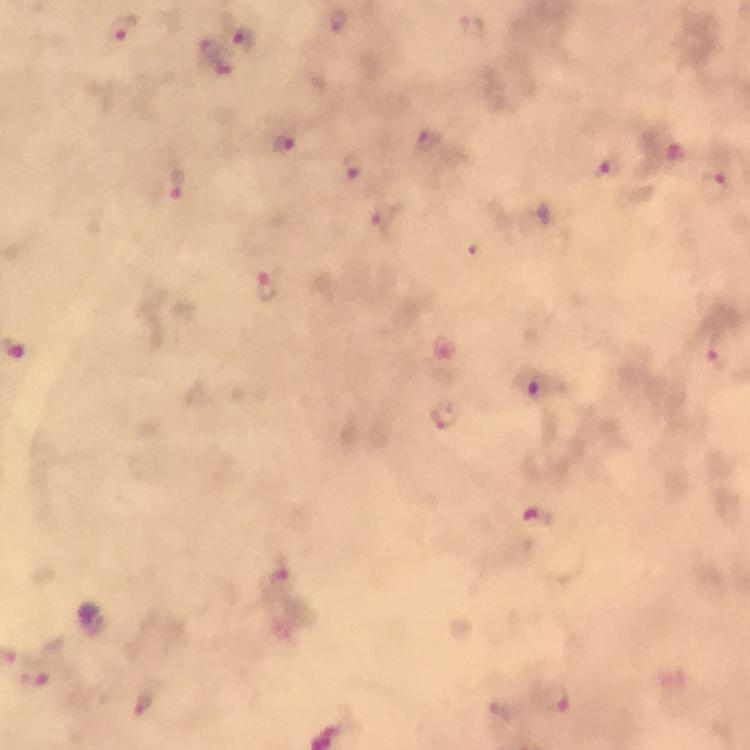

{
  "capture": "smartphone mounted on the microscope",
  "preparation": "thick smear",
  "magnification": "100x",
  "image_size": "750×750 pixels",
  "malaria_parasite_locations": "approximate centers as (x, y) in pixels: (336, 21), (126, 27), (243, 40), (425, 137), (285, 144), (672, 149), (354, 164), (604, 168), (718, 176), (178, 185), (269, 285), (541, 384), (445, 415), (538, 519), (278, 582), (556, 698), (144, 701)",
  "context": "from a malaria diagnostic workup",
  "cropped_from": "one field of view",
  "stain": "Giemsa",
  "immersion_oil": "applied"
}